Give the position of every malaria parasite.
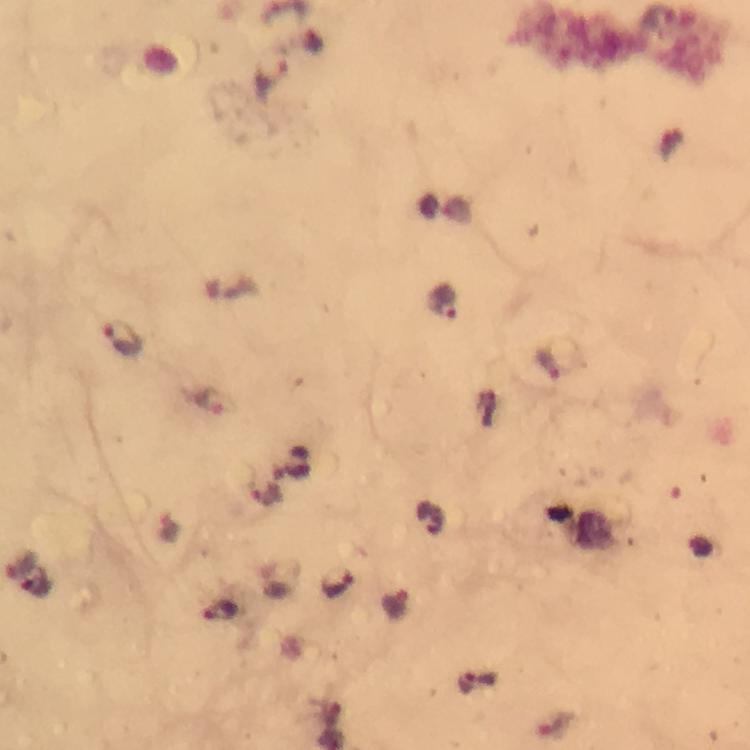

Approximate centers as (x, y) in pixels.
Malaria parasites: (660, 19), (273, 73), (441, 302), (122, 339), (549, 363), (209, 402), (265, 493), (430, 517), (36, 583), (336, 583), (395, 604), (221, 612), (476, 682).

Summary:
  - Image size: 750×750 pixels
  - Stain: Giemsa
  - Magnification: 100x
  - Immersion oil: used
  - Context: from a malaria diagnostic workup
  - Capture: smartphone mounted on the microscope
  - Cropped from: one field of view
  - Preparation: thick smear